Locate every Plasmodium parasite.
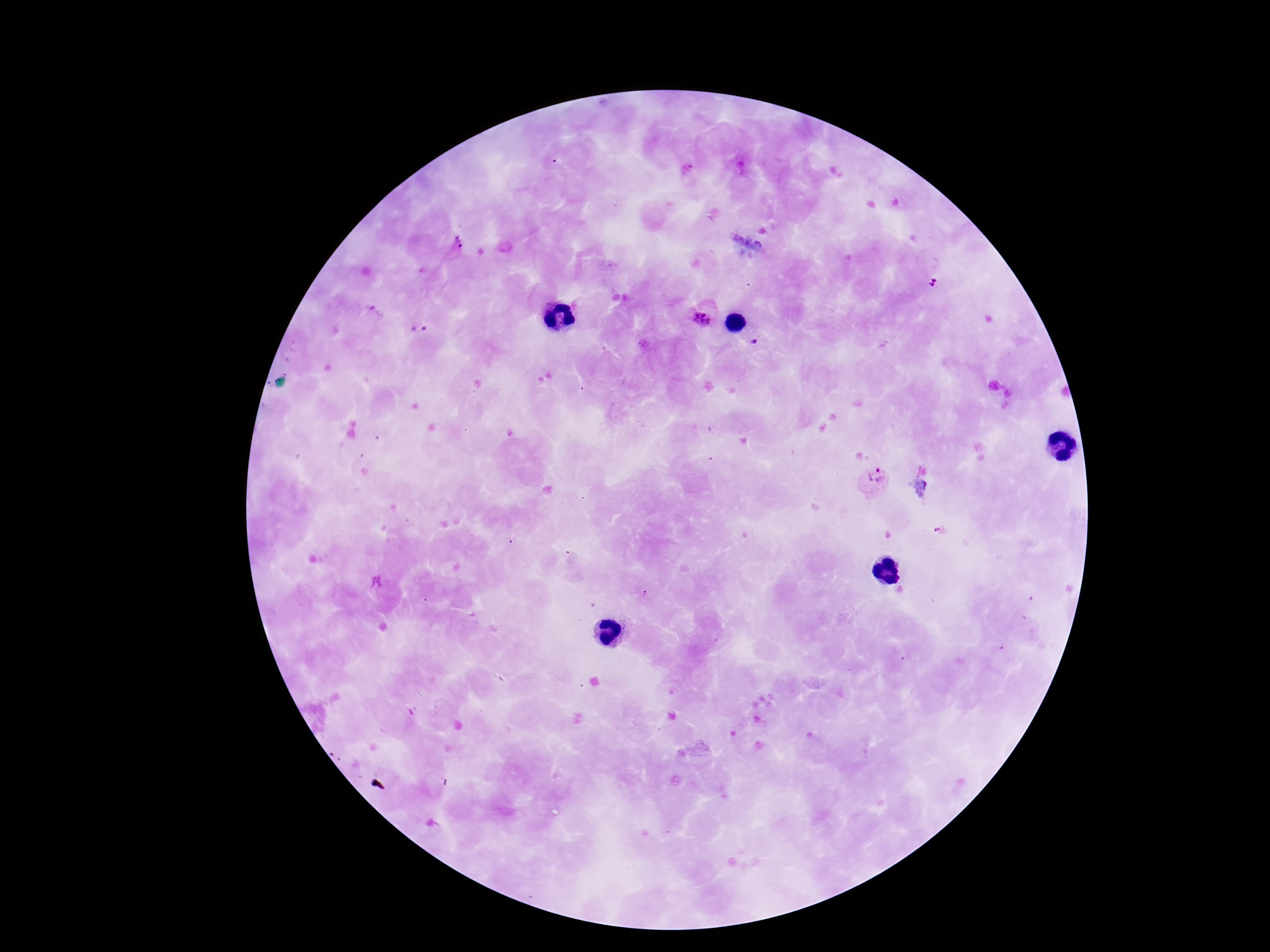

Approximate centers as (x, y) in pixels.
Plasmodium parasites: (456, 243), (704, 318), (419, 326), (753, 342), (872, 482).

One field from this slide. Image is 1270×952 pixels. Thick blood smear. Patient malaria status: infected. Photographed through the microscope eyepiece with a smartphone camera. 100x magnification. Giemsa stain.